Name the parasite shown.
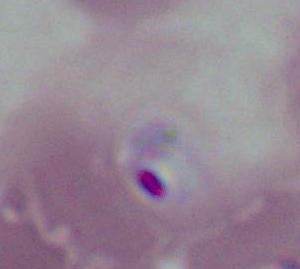
This is Plasmodium.

Micrograph. 400x or 1000x magnification.